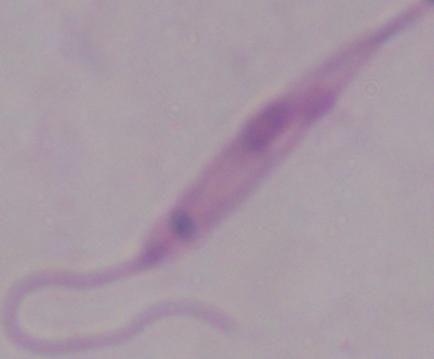

Summary:
  - Modality: photomicrograph
  - Magnification: 1000x
  - Identification: Leishmania